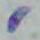 Toxoplasma gondii is seen. Micrograph. Captured at 1000x magnification.